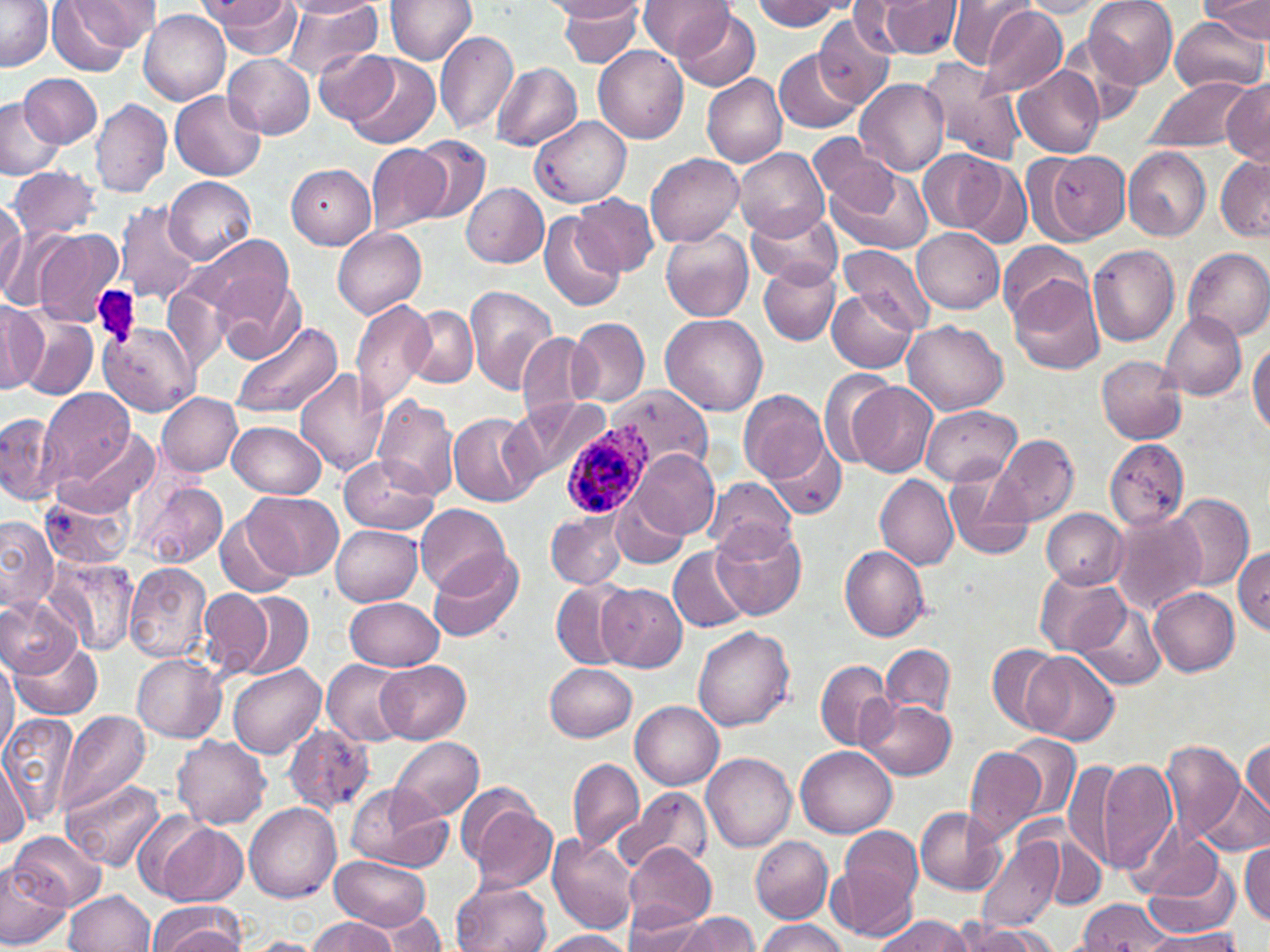 Approximate bounding boxes as (x1,y1)-(x2,y2) corner pairs in pixels. Plasmodium ovale-infected red blood cell locations: (560,421)-(650,520). Uninfected red blood cell locations: (205,0)-(300,55), (277,0)-(382,80), (280,0)-(380,18), (385,0)-(478,64), (548,0)-(642,23), (636,0)-(731,58), (878,0)-(963,58), (947,0)-(1034,71), (1086,0)-(1178,86), (1198,0)-(1270,38), (753,1)-(847,30), (1017,1)-(1112,17), (0,2)-(54,71), (51,2)-(145,69), (559,2)-(644,67), (847,3)-(920,54), (977,6)-(1069,99), (675,7)-(761,91), (139,11)-(230,105), (814,14)-(896,106), (1166,18)-(1265,94), (435,28)-(519,137), (1059,35)-(1150,119), (593,44)-(688,143), (315,48)-(399,125), (774,50)-(862,133), (224,54)-(313,138), (346,55)-(438,149), (917,57)-(1027,163), (493,62)-(581,150), (1012,64)-(1104,158), (701,72)-(788,168), (20,73)-(100,148), (1145,76)-(1253,152), (855,79)-(949,176), (1220,79)-(1270,162), (172,89)-(266,181), (0,96)-(65,180), (90,99)-(172,198), (531,116)-(631,207), (809,132)-(899,218), (412,134)-(490,224), (366,142)-(448,239), (735,147)-(829,240), (1123,147)-(1210,241), (917,150)-(1005,234), (1047,151)-(1129,241), (644,153)-(744,248), (1216,155)-(1269,242), (950,156)-(1033,250), (286,164)-(376,249), (9,166)-(99,241), (825,166)-(933,257), (165,176)-(258,264), (463,183)-(549,268), (571,193)-(659,276), (0,200)-(26,297), (113,200)-(201,306), (746,207)-(844,288), (540,211)-(626,312), (661,226)-(754,322), (333,227)-(426,318), (912,228)-(1005,313), (34,229)-(125,325), (185,233)-(293,323), (998,240)-(1090,323), (1088,244)-(1181,346), (839,245)-(932,336), (1184,247)-(1270,341), (758,262)-(841,346), (1009,271)-(1104,374), (215,274)-(307,363), (159,284)-(229,378), (466,284)-(559,394), (828,288)-(917,373), (0,299)-(47,392), (351,299)-(435,412), (402,304)-(479,386), (16,309)-(99,400), (1159,310)-(1248,400), (661,314)-(767,415), (567,315)-(650,409), (903,320)-(1008,415), (229,321)-(343,420), (99,324)-(197,415), (516,334)-(596,422), (1248,340)-(1270,436), (1097,357)-(1186,444), (818,368)-(903,467), (295,369)-(387,475), (848,381)-(938,477), (606,385)-(712,479), (39,387)-(135,487), (738,388)-(832,486), (157,392)-(242,476), (373,395)-(461,500), (509,399)-(611,491), (922,405)-(1020,485), (448,411)-(539,506), (0,412)-(66,506), (226,418)-(327,498), (59,431)-(159,516), (763,435)-(846,517), (991,435)-(1079,526), (1104,439)-(1191,531), (633,449)-(718,539), (338,454)-(440,534), (942,467)-(1036,562), (874,473)-(959,569), (703,477)-(797,559), (134,480)-(227,569), (246,491)-(343,579), (610,491)-(689,568), (41,492)-(133,570), (1169,492)-(1254,593), (415,504)-(511,596), (216,505)-(303,598), (1041,508)-(1129,587), (546,510)-(629,589), (1110,510)-(1208,615), (0,515)-(58,610), (713,522)-(806,620), (331,525)-(422,606), (669,545)-(751,633), (838,545)-(930,641), (1233,547)-(1270,635), (427,549)-(526,643), (45,556)-(140,658), (125,563)-(212,662), (1037,568)-(1132,657), (551,579)-(631,668), (597,582)-(687,672), (1149,587)-(1240,676), (200,588)-(274,679), (0,592)-(81,678), (239,593)-(313,678), (343,597)-(445,672), (1074,604)-(1168,691), (692,625)-(794,730), (9,637)-(103,721), (882,644)-(955,716), (989,645)-(1064,731), (1025,651)-(1120,746), (0,653)-(18,761), (132,655)-(227,743), (321,656)-(409,746), (814,659)-(897,750), (228,660)-(324,759), (376,661)-(470,744), (545,663)-(636,742), (862,698)-(956,780), (631,700)-(724,787), (56,710)-(152,821), (1,711)-(79,827), (282,724)-(376,815), (1004,733)-(1081,825), (173,735)-(272,831), (390,736)-(484,818), (1242,736)-(1270,818), (1161,740)-(1246,844), (795,744)-(898,836), (963,746)-(1051,842), (0,753)-(30,846), (704,753)-(796,852), (566,756)-(644,855), (1064,756)-(1121,869), (1096,757)-(1179,877), (64,779)-(164,872), (1201,780)-(1269,855), (345,783)-(451,872), (613,786)-(712,878), (461,793)-(559,893), (245,801)-(341,902), (913,805)-(1006,895), (147,819)-(249,907), (834,825)-(925,939), (9,829)-(104,910), (1134,833)-(1233,916), (976,834)-(1064,934), (748,835)-(832,922), (548,836)-(640,934), (1044,838)-(1104,911), (1241,840)-(1270,925), (622,846)-(717,933), (328,855)-(432,933), (0,858)-(70,947), (452,880)-(550,952), (63,890)-(154,952), (1077,899)-(1173,949), (147,901)-(246,952), (625,909)-(715,951), (381,911)-(449,951), (678,911)-(760,952), (873,915)-(976,952), (309,917)-(397,952), (757,920)-(847,952), (948,922)-(1058,952), (1133,928)-(1244,952), (538,930)-(633,952), (245,936)-(326,951). Platelet locations: (93,287)-(142,347). Slide-level diagnosis: Plasmodium ovale. Thin blood film. Single field of view. 1000x magnification. Image is 1270×952 pixels. Light microscopy. May-Grünwald-Giemsa-stained preparation.